Report the malaria status of this cell.
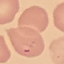

It is parasitized.

Cell patch, automatically extracted from a larger field of view and resized to 64 × 64 pixels. Acquired by smartphone through the microscope eyepiece. Thin blood smear. Giemsa-stained preparation.